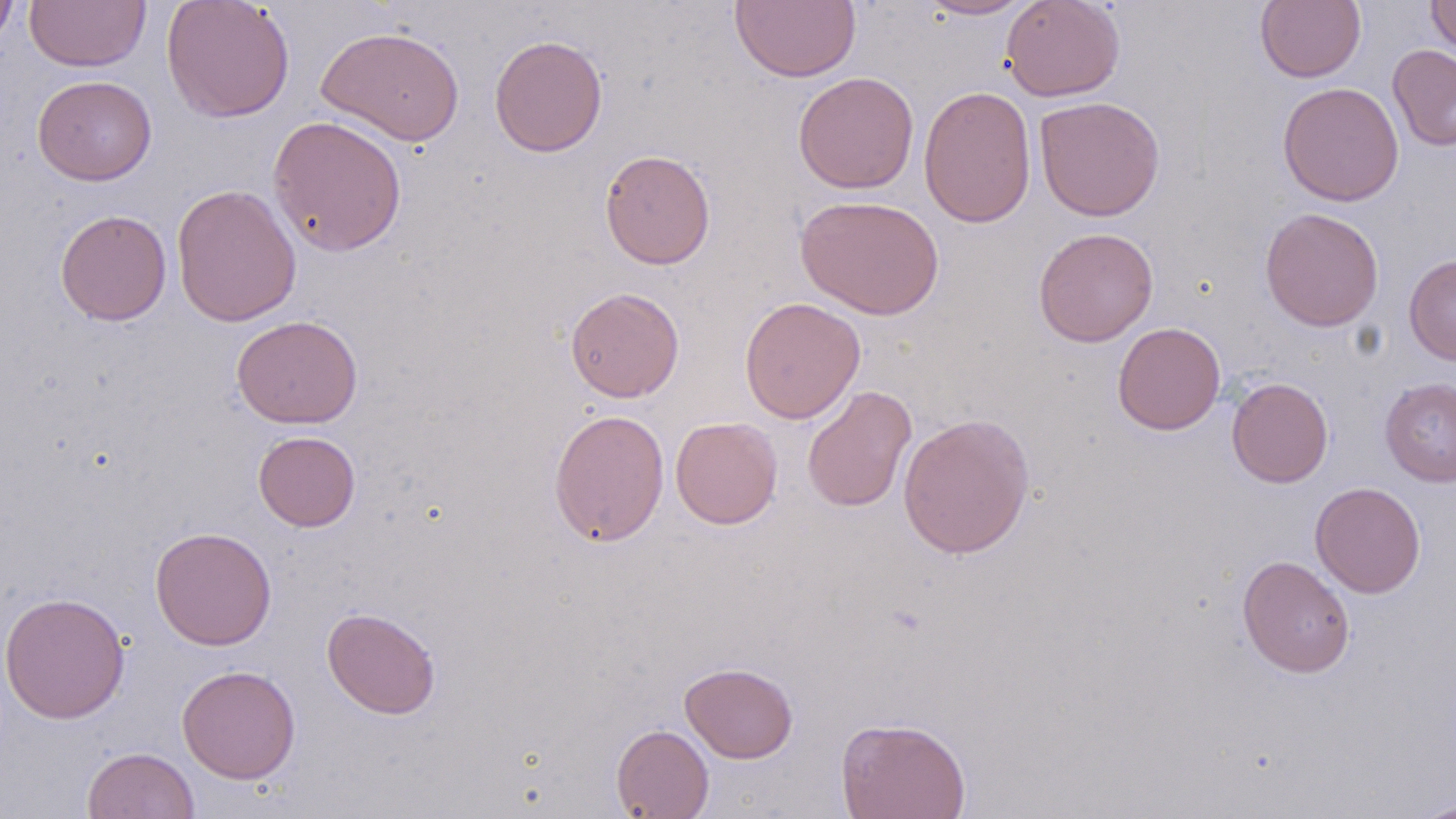
slide-level diagnosis = no evidence of blood parasites
magnification = 1000x
uninfected red blood cell locations = approximate bounding boxes as (x1,y1)-(x2,y2) corner pairs in pixels: (0,0)-(18,51), (25,0)-(151,72), (161,0)-(295,123), (729,0)-(861,83), (916,0)-(1033,20), (1000,0)-(1126,102), (1426,0)-(1456,59), (1255,1)-(1365,83), (315,26)-(465,146), (489,34)-(608,158), (1387,44)-(1456,151), (792,71)-(919,194), (32,75)-(157,185), (1277,82)-(1404,206), (918,85)-(1037,228), (1034,96)-(1165,221), (267,115)-(407,256), (599,149)-(716,269), (171,183)-(302,328), (795,194)-(945,320), (1260,207)-(1384,332), (55,209)-(171,326), (1033,227)-(1159,347), (1404,254)-(1456,365), (564,286)-(685,403), (739,297)-(865,423), (230,315)-(363,429), (1112,322)-(1226,435), (1226,377)-(1333,488), (1379,377)-(1456,486), (802,385)-(916,513), (548,408)-(670,547), (897,412)-(1036,559), (670,416)-(783,530), (253,430)-(361,531), (1310,481)-(1426,598), (150,526)-(277,650), (1237,555)-(1355,678), (0,591)-(130,724), (322,607)-(441,719), (680,662)-(798,763), (177,664)-(301,784), (836,716)-(971,819), (611,724)-(714,819), (83,746)-(200,819), (1410,800)-(1456,819)
field of view = single
preparation = thin blood smear
image size = 1456×819 pixels
stain = May-Grünwald-Giemsa
modality = optical microscopy